Report the malaria status of this cell.
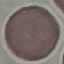
Uninfected.

stain: Giemsa
image_type: automatically extracted cell patch, resized to 64 × 64 pixels
preparation: thin smear
capture: smartphone through the microscope eyepiece